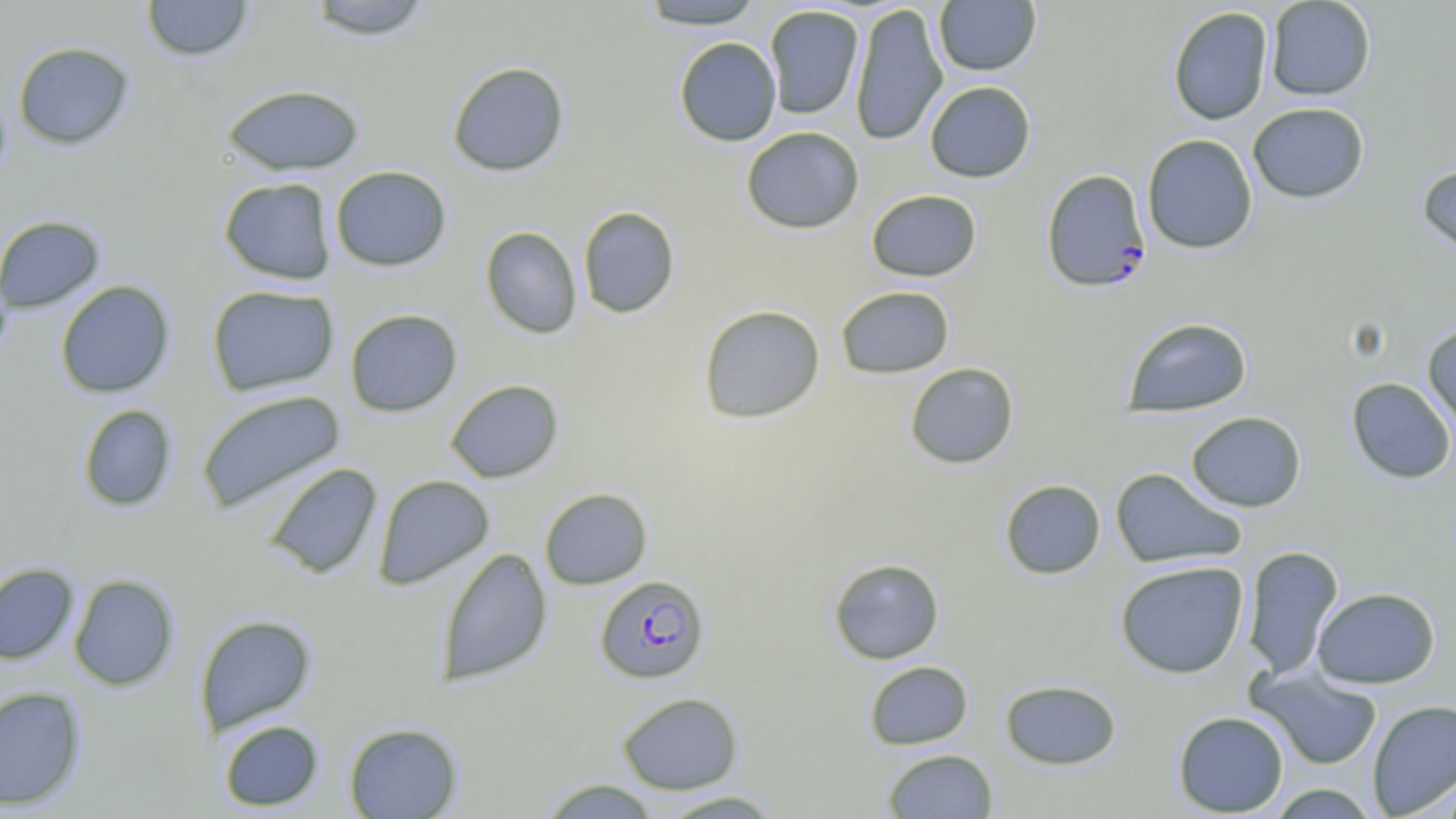
Summary:
  - Coordinate format: approximate bounding boxes as (x1,y1)-(x2,y2) corner pairs in pixels
  - Plasmodium falciparum-infected red blood cell locations: (1041,169)-(1151,293), (594,575)-(710,685)
  - Uninfected red blood cell locations: (141,0)-(254,62), (302,0)-(436,41), (933,0)-(1041,76), (1265,0)-(1376,100), (636,1)-(768,30), (849,2)-(948,146), (763,5)-(864,120), (1167,6)-(1274,126), (673,37)-(782,146), (12,41)-(134,149), (447,61)-(570,177), (924,81)-(1036,183), (221,84)-(365,176), (1247,102)-(1369,203), (741,126)-(865,234), (1141,134)-(1258,254), (1417,161)-(1456,263), (330,165)-(452,271), (218,177)-(337,286), (865,189)-(983,282), (578,206)-(680,318), (0,215)-(105,312), (480,226)-(583,338), (55,280)-(175,398), (206,285)-(340,396), (835,285)-(954,379), (697,304)-(825,424), (344,308)-(463,417), (1121,316)-(1253,418), (1422,322)-(1456,430), (904,362)-(1019,469), (1346,377)-(1456,484), (445,379)-(564,483), (196,388)-(346,515), (77,404)-(177,511), (1186,411)-(1307,512), (263,463)-(382,580), (1110,467)-(1246,570), (373,474)-(495,590), (999,479)-(1106,580), (539,487)-(653,590), (1241,546)-(1345,680), (436,547)-(552,686), (828,558)-(945,664), (1114,560)-(1249,679), (0,563)-(79,665), (68,574)-(180,691), (1312,586)-(1441,689), (194,614)-(317,734), (863,660)-(974,750), (1248,667)-(1383,771), (999,679)-(1122,770), (0,685)-(87,810), (617,691)-(744,794), (1367,699)-(1456,818), (1172,710)-(1289,817), (218,719)-(324,811), (343,722)-(463,818), (882,748)-(998,818), (1435,770)-(1456,818), (537,778)-(662,818), (1263,783)-(1382,818), (653,790)-(788,818)
  - Slide-level diagnosis: Plasmodium falciparum
  - Image size: 1456×819 pixels
  - Preparation: thin blood film
  - Field of view: one of a larger specimen
  - Magnification: 1000x
  - Stain: May-Grünwald-Giemsa
  - Modality: light microscopy